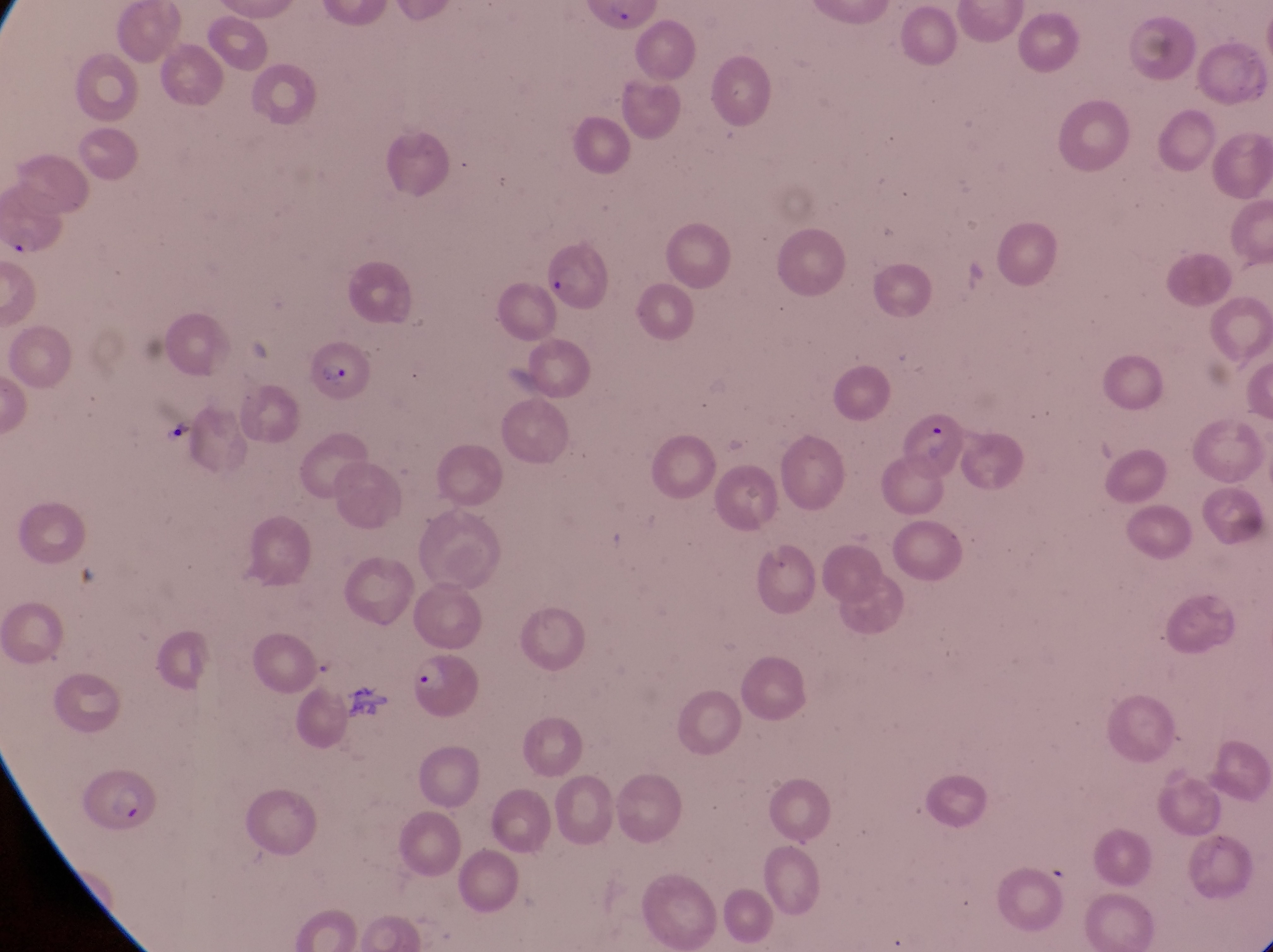

Approximate bounding boxes as [left, top, right, bottom] in pixels.
Summary:
  - Parasitised red blood cell locations: [3, 182, 78, 272], [547, 242, 607, 314], [304, 337, 369, 402], [908, 396, 965, 498], [412, 656, 484, 724], [80, 769, 158, 841]
  - Field of view: single
  - Preparation: thin blood smear
  - Image size: 1273×952 pixels
  - Magnification: 1000x
  - Capture: smartphone photograph through the eyepiece of an Olympus CX-23 microscope
  - Country: Uganda